Assess for malaria.
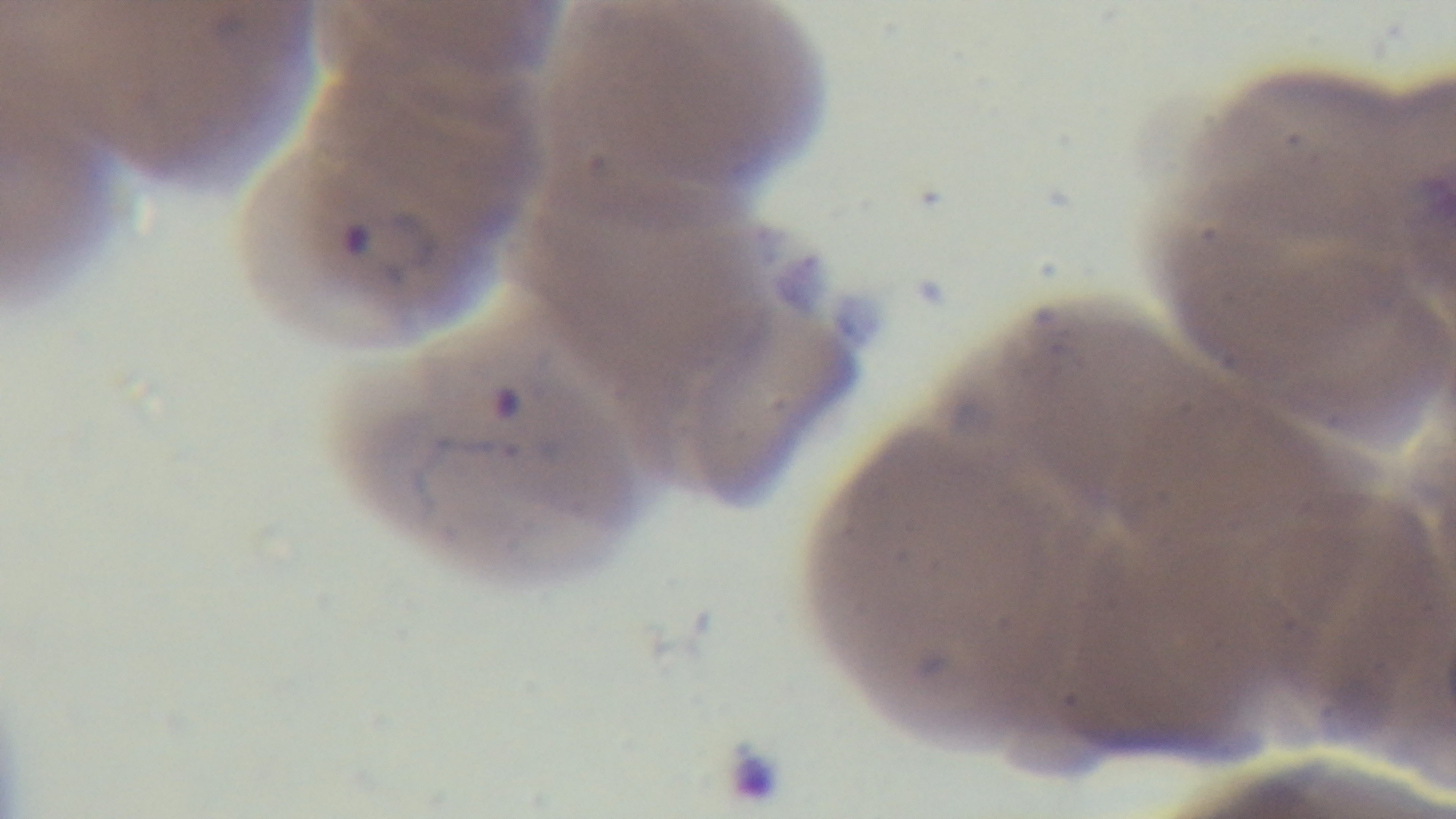
Positive.

capture = mounted 4K digital camera
stain = Giemsa
objective = 100x oil immersion
preparation = thin
field of view = single
modality = light microscopy